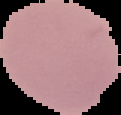

image size = 121×115 pixels
preparation = thin blood smear
image type = segmented cell region with the area outside set to black
result = no malaria parasites seen